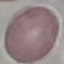
Malaria status: uninfected. Automatically extracted cell patch, resized to 64 × 64 pixels. Thin blood smear. Photographed with a smartphone camera at the microscope eyepiece. Giemsa stain.